Locate and identify every blood parasite.
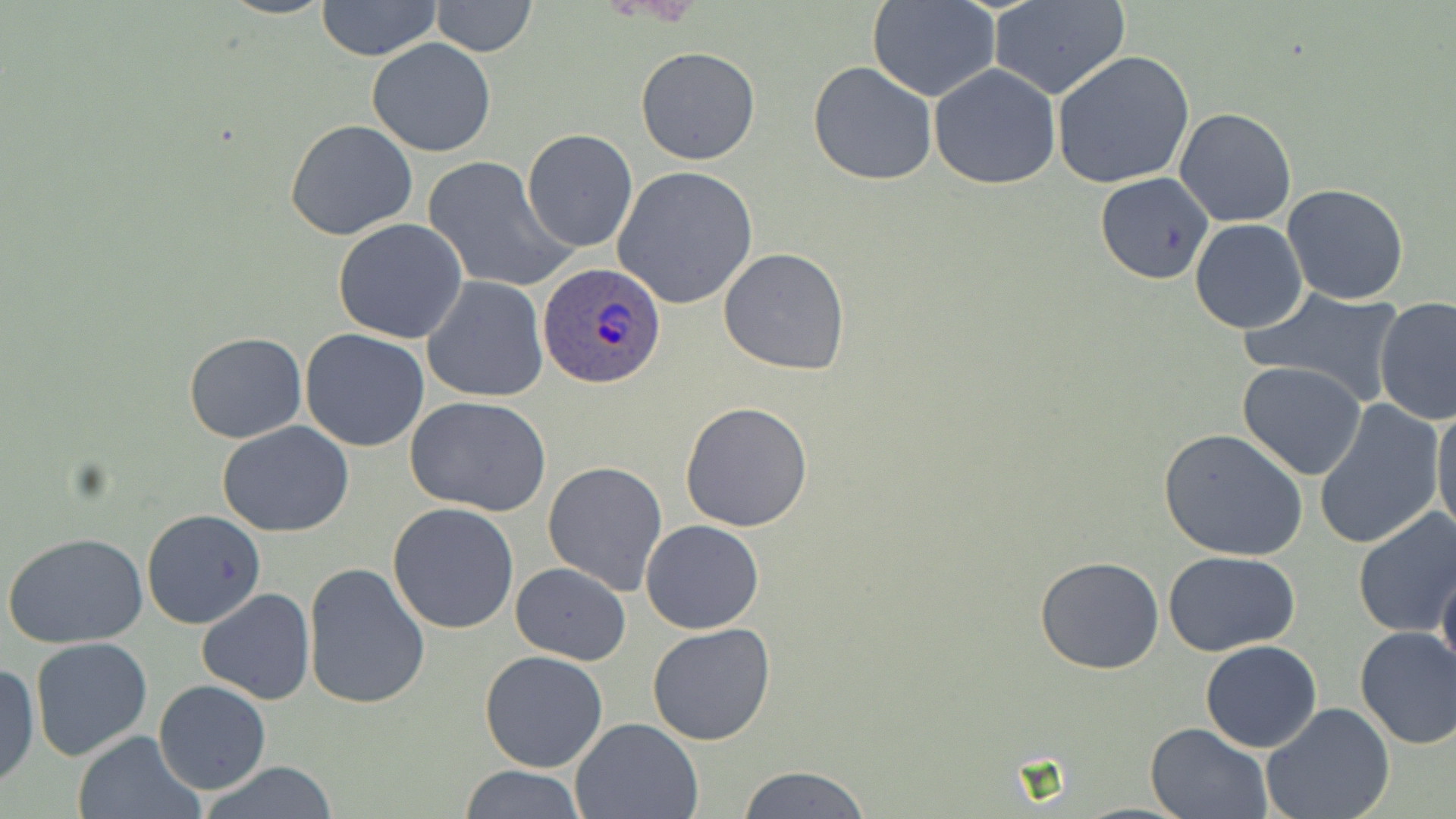

Approximate bounding boxes as named x1/y1/x2/y2 corners in pixels.
Plasmodium ovale-infected red blood cells: (x1=539, y1=261, x2=665, y2=389).
No Plasmodium falciparum, Plasmodium malariae, Plasmodium vivax, Babesia divergens, or Trypanosoma brucei observed.

Uninfected red blood cell locations: (x1=316, y1=0, x2=439, y2=59), (x1=867, y1=0, x2=1002, y2=102), (x1=429, y1=1, x2=538, y2=57), (x1=988, y1=1, x2=1128, y2=101), (x1=367, y1=38, x2=496, y2=156), (x1=635, y1=47, x2=760, y2=164), (x1=1051, y1=50, x2=1196, y2=191), (x1=807, y1=60, x2=938, y2=186), (x1=927, y1=64, x2=1061, y2=189), (x1=1173, y1=108, x2=1297, y2=228), (x1=285, y1=118, x2=418, y2=241), (x1=521, y1=128, x2=638, y2=253), (x1=422, y1=155, x2=575, y2=293), (x1=612, y1=166, x2=758, y2=309), (x1=1096, y1=172, x2=1215, y2=286), (x1=1281, y1=183, x2=1409, y2=305), (x1=333, y1=219, x2=468, y2=344), (x1=1189, y1=219, x2=1308, y2=334), (x1=719, y1=247, x2=851, y2=377), (x1=421, y1=276, x2=548, y2=403), (x1=1240, y1=287, x2=1404, y2=408), (x1=1372, y1=296, x2=1456, y2=428), (x1=300, y1=329, x2=430, y2=452), (x1=183, y1=332, x2=308, y2=443), (x1=1237, y1=363, x2=1368, y2=480), (x1=404, y1=396, x2=551, y2=515), (x1=1431, y1=400, x2=1456, y2=540), (x1=681, y1=401, x2=814, y2=533), (x1=1313, y1=401, x2=1445, y2=551), (x1=217, y1=422, x2=354, y2=536), (x1=1158, y1=427, x2=1308, y2=562), (x1=543, y1=461, x2=669, y2=595), (x1=388, y1=502, x2=520, y2=634), (x1=143, y1=510, x2=264, y2=631), (x1=1352, y1=510, x2=1456, y2=637), (x1=640, y1=520, x2=765, y2=634), (x1=3, y1=531, x2=149, y2=647), (x1=1163, y1=551, x2=1301, y2=657), (x1=1034, y1=556, x2=1165, y2=674), (x1=1436, y1=560, x2=1456, y2=678), (x1=302, y1=561, x2=431, y2=709), (x1=510, y1=562, x2=631, y2=667), (x1=197, y1=587, x2=315, y2=705), (x1=647, y1=623, x2=776, y2=747), (x1=1352, y1=625, x2=1456, y2=749), (x1=30, y1=638, x2=153, y2=760), (x1=1199, y1=640, x2=1323, y2=753), (x1=478, y1=650, x2=609, y2=773), (x1=1220, y1=656, x2=1364, y2=787), (x1=0, y1=661, x2=38, y2=791), (x1=154, y1=680, x2=271, y2=794), (x1=1262, y1=703, x2=1395, y2=819), (x1=572, y1=717, x2=702, y2=819), (x1=1144, y1=721, x2=1274, y2=818), (x1=71, y1=730, x2=203, y2=819), (x1=197, y1=761, x2=345, y2=819), (x1=456, y1=764, x2=584, y2=819), (x1=735, y1=765, x2=874, y2=819). Slide-level diagnosis: Plasmodium ovale. Image is 1456×819 pixels. Single field of view. Captured at 1000x magnification. Thin blood film. Light microscopy. May-Grünwald-Giemsa-stained preparation.